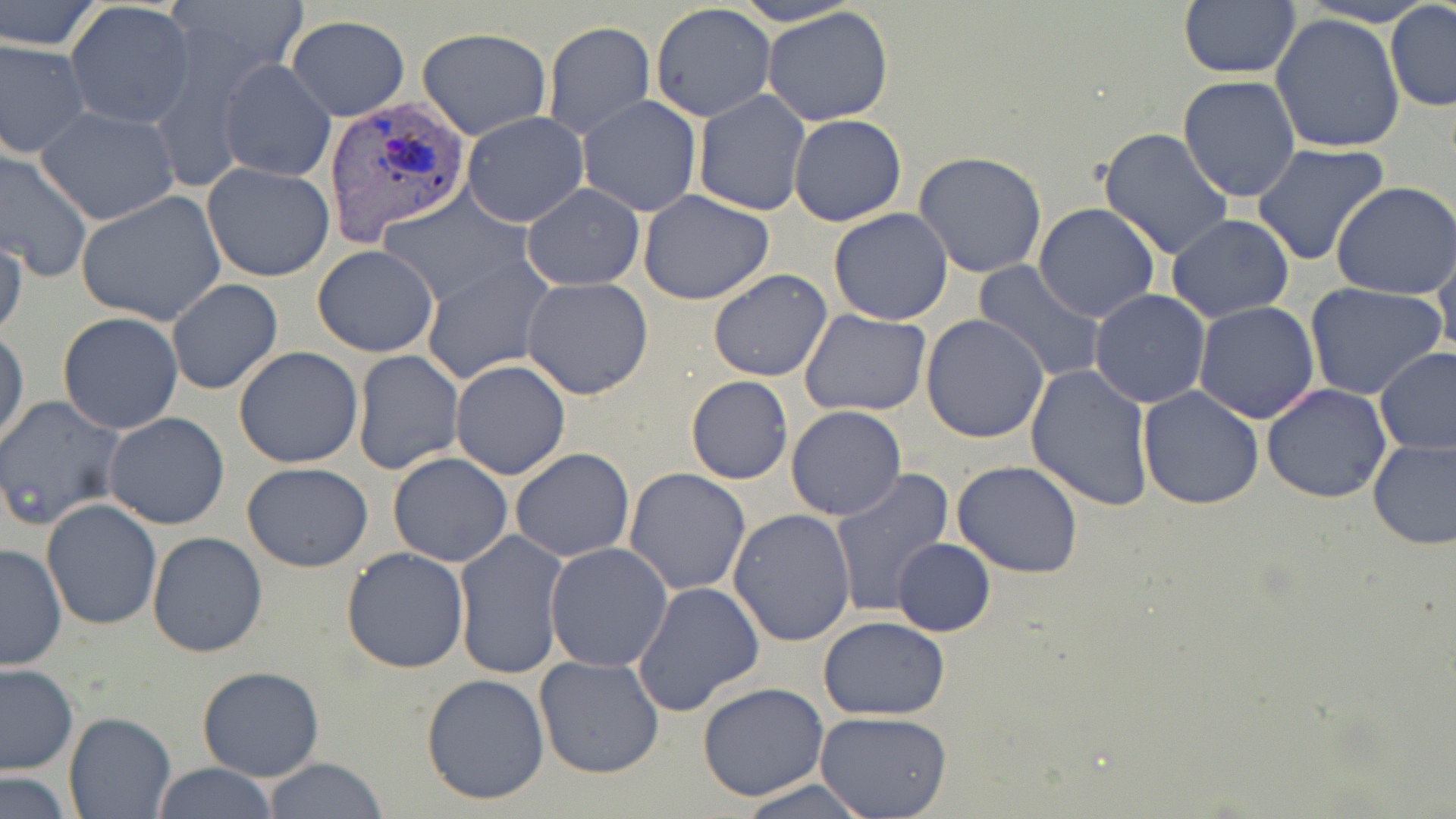
Approximate bounding boxes as named x1/y1/x2/y2 corners in pixels. Plasmodium vivax-infected red blood cell locations: (x1=320, y1=95, x2=471, y2=249). Uninfected red blood cell locations: (x1=0, y1=0, x2=104, y2=53), (x1=728, y1=0, x2=862, y2=27), (x1=1298, y1=0, x2=1438, y2=26), (x1=1178, y1=1, x2=1301, y2=78), (x1=65, y1=2, x2=194, y2=128), (x1=650, y1=2, x2=777, y2=123), (x1=1385, y1=3, x2=1456, y2=111), (x1=762, y1=6, x2=895, y2=127), (x1=1271, y1=13, x2=1405, y2=156), (x1=285, y1=15, x2=409, y2=121), (x1=542, y1=22, x2=656, y2=138), (x1=416, y1=27, x2=552, y2=141), (x1=0, y1=38, x2=90, y2=158), (x1=217, y1=57, x2=336, y2=183), (x1=1177, y1=75, x2=1301, y2=203), (x1=693, y1=89, x2=809, y2=216), (x1=577, y1=95, x2=701, y2=217), (x1=36, y1=104, x2=179, y2=226), (x1=460, y1=112, x2=588, y2=227), (x1=788, y1=114, x2=907, y2=226), (x1=1097, y1=127, x2=1234, y2=261), (x1=1251, y1=142, x2=1390, y2=266), (x1=0, y1=148, x2=95, y2=283), (x1=914, y1=151, x2=1048, y2=279), (x1=201, y1=162, x2=334, y2=282), (x1=1331, y1=181, x2=1456, y2=299), (x1=522, y1=183, x2=645, y2=291), (x1=75, y1=189, x2=227, y2=325), (x1=379, y1=189, x2=526, y2=304), (x1=639, y1=190, x2=775, y2=305), (x1=1032, y1=202, x2=1162, y2=323), (x1=829, y1=207, x2=954, y2=325), (x1=1167, y1=215, x2=1294, y2=323), (x1=0, y1=229, x2=26, y2=341), (x1=1433, y1=239, x2=1456, y2=362), (x1=311, y1=244, x2=439, y2=357), (x1=422, y1=256, x2=555, y2=385), (x1=974, y1=260, x2=1106, y2=384), (x1=708, y1=269, x2=833, y2=381), (x1=521, y1=277, x2=654, y2=400), (x1=167, y1=278, x2=282, y2=394), (x1=1302, y1=282, x2=1448, y2=402), (x1=1089, y1=289, x2=1212, y2=408), (x1=1194, y1=302, x2=1321, y2=423), (x1=800, y1=309, x2=932, y2=417), (x1=57, y1=311, x2=185, y2=434), (x1=921, y1=313, x2=1050, y2=443), (x1=0, y1=329, x2=27, y2=449), (x1=233, y1=346, x2=364, y2=468), (x1=1374, y1=346, x2=1455, y2=455), (x1=352, y1=350, x2=463, y2=475), (x1=450, y1=360, x2=571, y2=480), (x1=1025, y1=364, x2=1154, y2=510), (x1=686, y1=375, x2=793, y2=484), (x1=1261, y1=383, x2=1391, y2=503), (x1=1136, y1=385, x2=1265, y2=511), (x1=0, y1=394, x2=126, y2=529), (x1=786, y1=406, x2=906, y2=519), (x1=103, y1=412, x2=231, y2=530), (x1=1367, y1=434, x2=1455, y2=550), (x1=511, y1=448, x2=635, y2=562), (x1=388, y1=452, x2=512, y2=567), (x1=951, y1=459, x2=1084, y2=578), (x1=241, y1=463, x2=374, y2=572), (x1=829, y1=467, x2=954, y2=619), (x1=623, y1=468, x2=751, y2=597), (x1=42, y1=499, x2=162, y2=632), (x1=728, y1=510, x2=857, y2=647), (x1=453, y1=529, x2=569, y2=681), (x1=147, y1=531, x2=268, y2=659), (x1=892, y1=538, x2=995, y2=637), (x1=0, y1=542, x2=68, y2=671), (x1=545, y1=542, x2=673, y2=671), (x1=341, y1=547, x2=470, y2=673), (x1=633, y1=582, x2=766, y2=718), (x1=819, y1=617, x2=950, y2=720), (x1=535, y1=654, x2=664, y2=779), (x1=0, y1=663, x2=78, y2=775), (x1=196, y1=666, x2=325, y2=781), (x1=421, y1=674, x2=550, y2=806), (x1=696, y1=681, x2=831, y2=803), (x1=64, y1=711, x2=175, y2=817), (x1=815, y1=712, x2=952, y2=819), (x1=262, y1=757, x2=389, y2=819), (x1=151, y1=762, x2=279, y2=818), (x1=0, y1=773, x2=74, y2=818), (x1=733, y1=777, x2=879, y2=818). Slide-level diagnosis: Plasmodium vivax. One field of a larger specimen. Optical microscopy. May-Grünwald-Giemsa-stained preparation. Thin blood smear. Captured at 1000x magnification. Image is 1456×819 pixels.